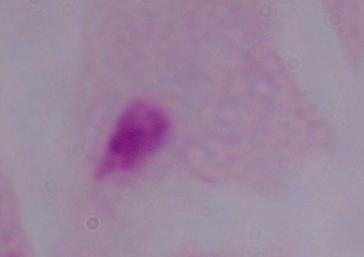 Micrograph. 1000x magnification. A trichomonad is shown.